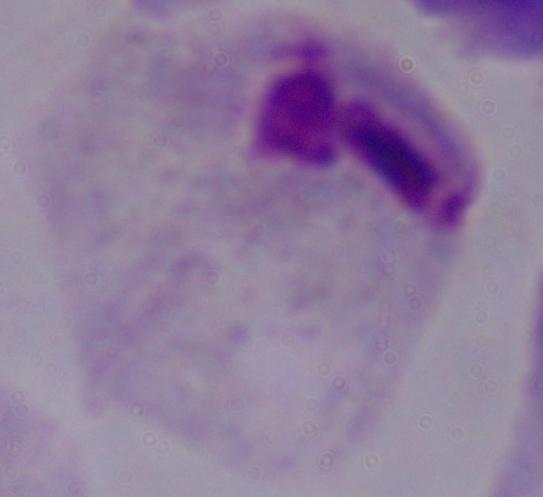

Micrograph. Captured at 1000x magnification. A trichomonad is shown.